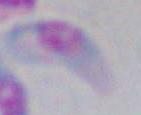
Summary:
  - Modality: micrograph
  - Magnification: 1000x
  - Identification: Toxoplasma gondii